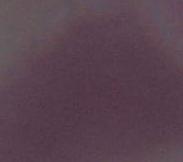 Photomicrograph. Captured at 1000x magnification. An erythrocyte is shown.